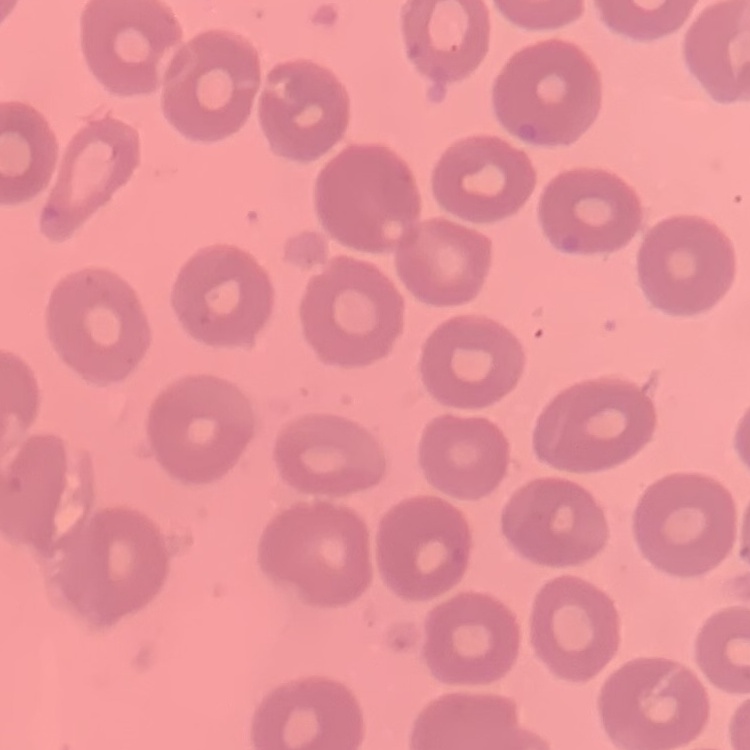

The erythrocytes show no rouleaux formation. Square crop of a larger photomicrograph. Stained with either Field's or Giemsa. Thin blood film.